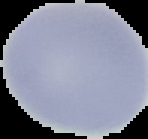

Summary:
  - Result: no malaria parasites seen
  - Image size: 148×139 pixels
  - Preparation: thin blood film
  - Image type: cell region segmented out of the field of view; surrounding area masked to black